State which cell type is depicted.
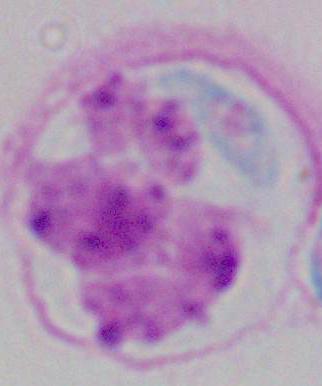
A leukocyte.

Photomicrograph. 1000x magnification.